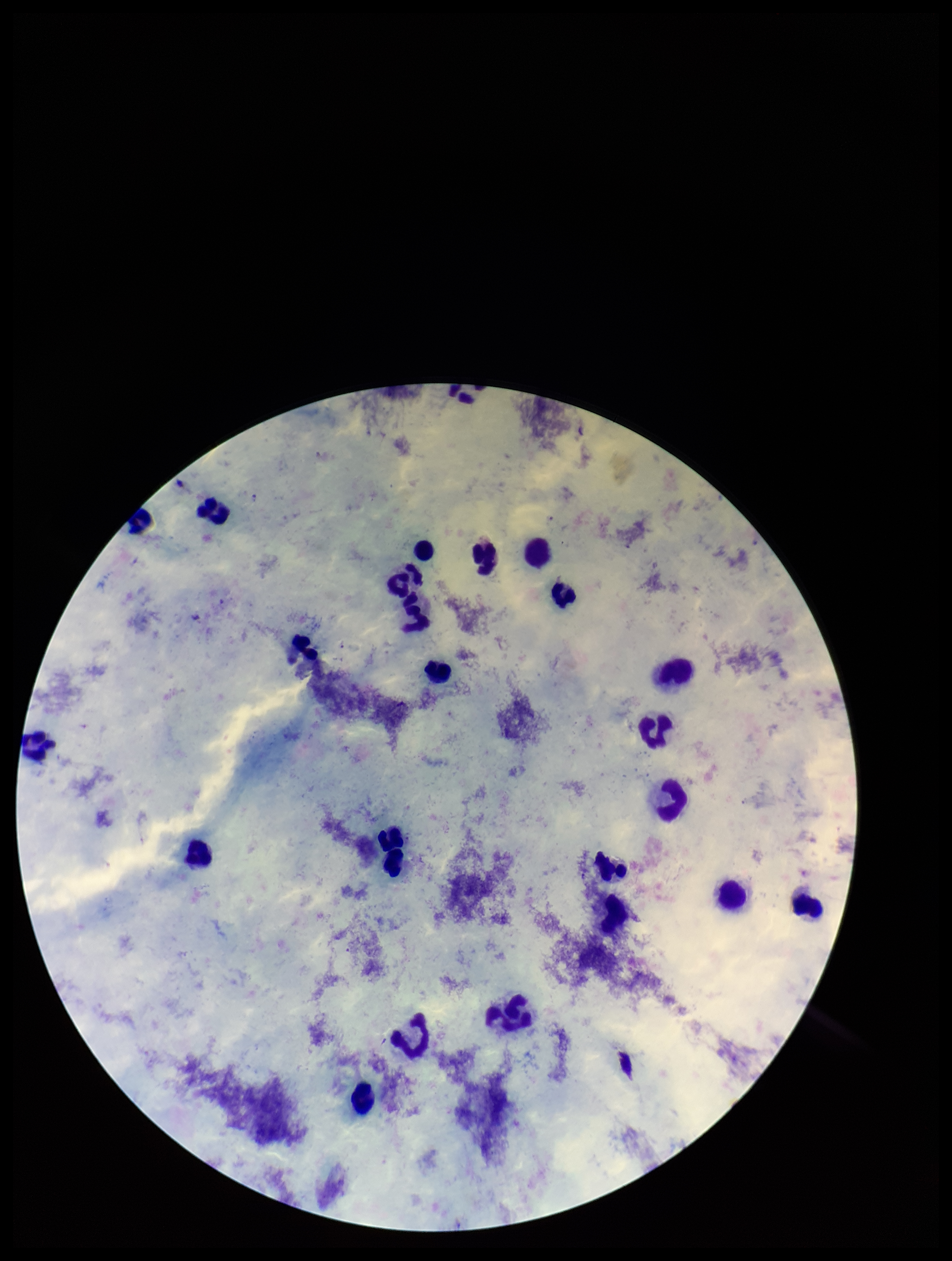 Smartphone photograph taken through the eyepiece of a microscope. Preparation: thick. Patient malaria status: positive. Image is 952×1261 pixels. Parasite count: 2. Species reported for this patient: Plasmodium falciparum. Plasmodium parasites: detected. Stained with Giemsa. Leukocyte count: 23. One field from this slide.